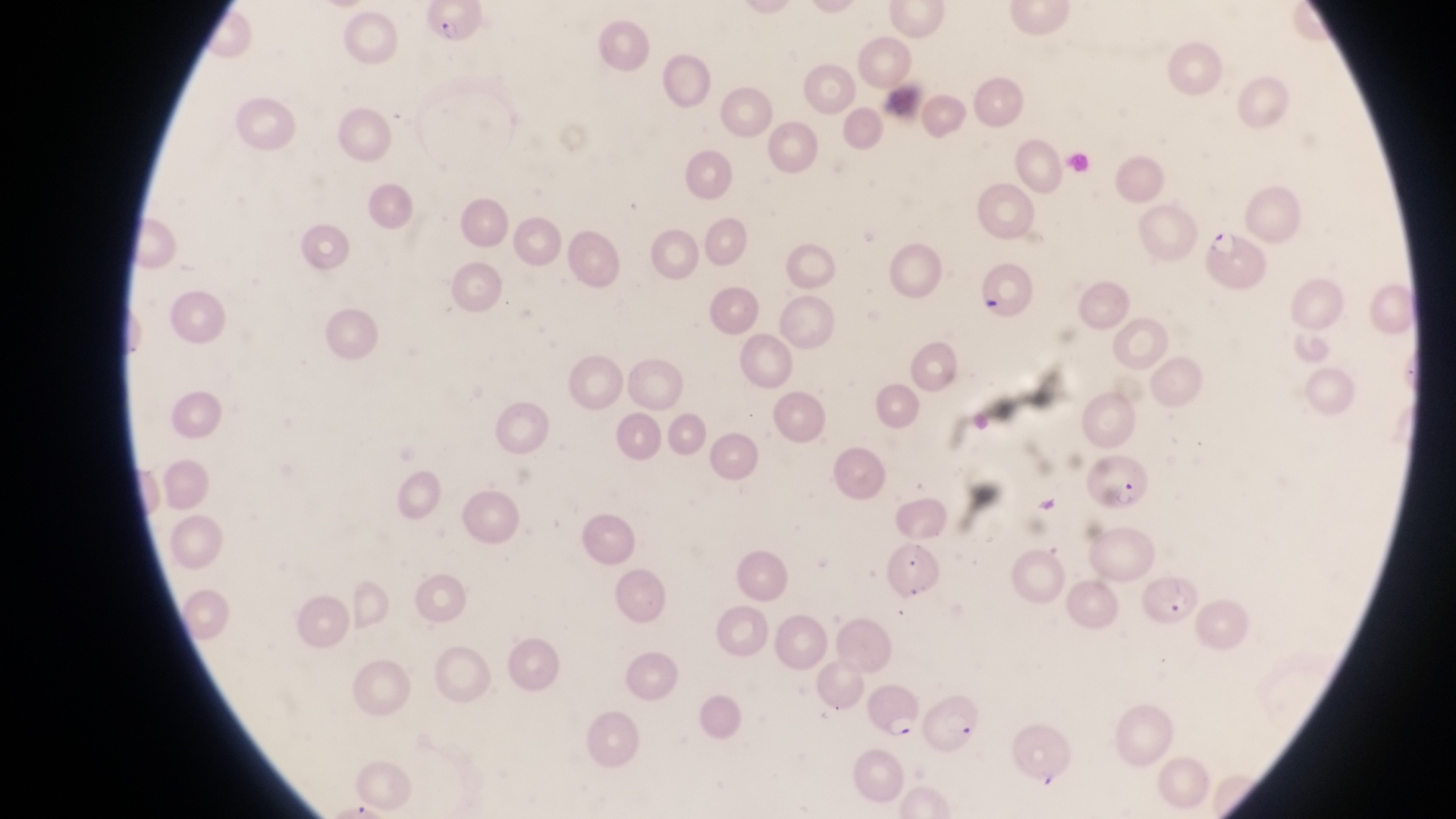

country = Uganda
capture = smartphone photograph through the eyepiece of an Olympus CX-23 microscope
artifact (platelet-like body, stain precipitate, or debris) locations = approximate bounding boxes as {left, top, right, bottom} in pixels: {979, 297, 1003, 315}
image size = 1456×819 pixels
magnification = 1000x
parasitised red blood cell locations = approximate bounding boxes as {left, top, right, bottom} in pixels: {422, 2, 489, 48}, {1200, 221, 1269, 293}, {1084, 455, 1153, 514}, {882, 536, 940, 600}, {1142, 571, 1200, 623}, {864, 680, 922, 739}, {922, 690, 985, 757}
preparation = thin blood smear
field of view = single